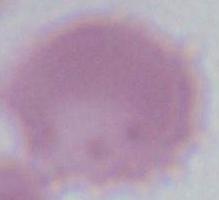 A red blood cell is shown. 1000x magnification. Photomicrograph.